State the blood parasite species.
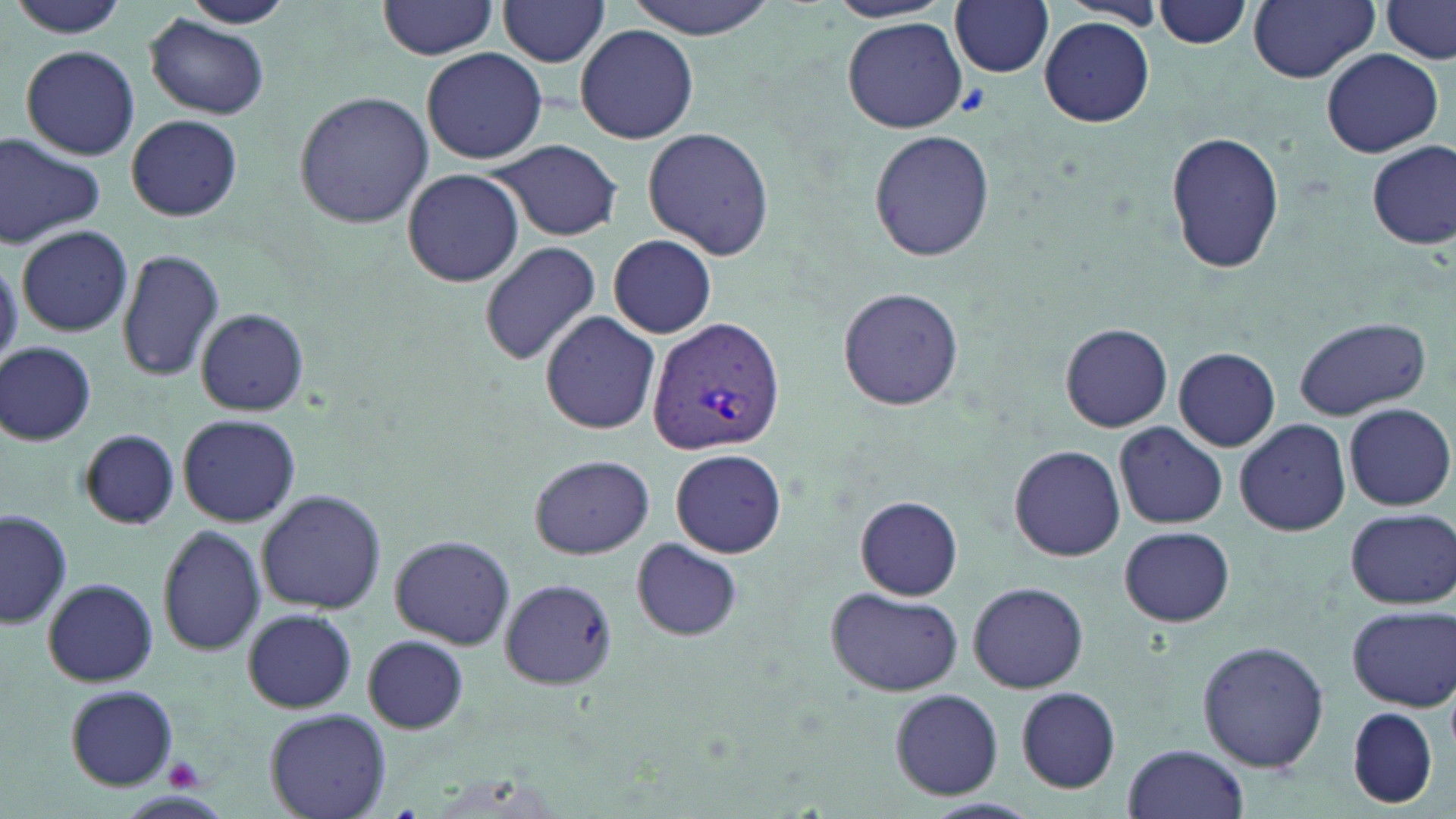

Plasmodium vivax.

field of view = single
platelet locations = approximate bounding boxes as (x1,y1)-(x2,y2) corner pairs in pixels: (167,759)-(206,792)
magnification = 1000x
preparation = thin blood smear
uninfected red blood cell locations = approximate bounding boxes as (x1,y1)-(x2,y2) corner pairs in pixels: (178,0)-(294,29), (622,0)-(780,38), (1154,0)-(1253,49), (1248,0)-(1378,84), (378,1)-(504,61), (495,1)-(612,66), (826,1)-(954,23), (1383,1)-(1455,62), (10,2)-(129,38), (951,2)-(1055,77), (147,14)-(274,121), (1040,16)-(1156,127), (842,17)-(966,131), (575,24)-(698,143), (20,45)-(141,161), (420,47)-(547,165), (1320,48)-(1444,157), (294,89)-(434,231), (126,114)-(242,221), (642,127)-(774,260), (869,129)-(996,263), (1166,131)-(1285,274), (0,135)-(105,247), (490,140)-(623,240), (1367,140)-(1455,250), (402,169)-(524,287), (17,224)-(134,338), (607,234)-(717,339), (478,240)-(602,368), (117,247)-(224,382), (0,254)-(22,370), (837,285)-(965,411), (196,308)-(307,417), (539,311)-(660,433), (1293,317)-(1430,421), (1060,322)-(1173,433), (1,343)-(97,446), (1172,347)-(1280,452), (1344,402)-(1454,511), (178,413)-(300,528), (1235,417)-(1351,536), (1113,423)-(1227,530), (78,430)-(179,530), (1008,445)-(1126,563), (671,449)-(786,558), (528,453)-(653,560), (257,488)-(387,614), (855,496)-(963,600), (1,507)-(71,632), (1345,508)-(1455,608), (157,524)-(265,656), (1119,526)-(1235,627), (390,536)-(514,649), (632,539)-(745,642), (42,578)-(158,687), (497,578)-(617,689), (967,581)-(1089,693), (826,586)-(963,697), (1345,605)-(1455,711), (242,608)-(357,712), (363,634)-(468,734), (1197,640)-(1330,774), (66,686)-(179,789), (1015,687)-(1119,791), (889,688)-(1005,802), (265,707)-(391,819), (1348,709)-(1439,808), (1122,743)-(1250,819)
image size = 1456×819 pixels
modality = light microscopy
Plasmodium vivax-infected red blood cell locations = approximate bounding boxes as (x1,y1)-(x2,y2) corner pairs in pixels: (648,315)-(786,455)
stain = May-Grünwald-Giemsa